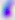
Summary:
  - Modality: photomicrograph
  - Identification: Toxoplasma gondii
  - Magnification: 400x